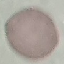
Summary:
  - Malaria status: uninfected
  - Preparation: thin blood film
  - Capture: smartphone through the microscope eyepiece
  - Stain: Giemsa
  - Image type: cell patch, automatically extracted from a larger field of view and resized to 64 × 64 pixels